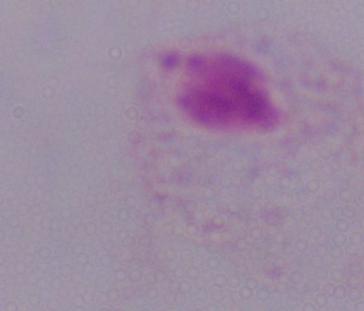

Summary:
  - Modality: photomicrograph
  - Identification: trichomonad
  - Magnification: 1000x